Identify the parasite.
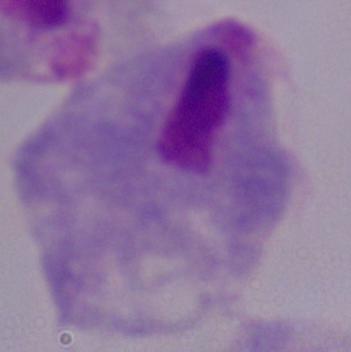
This is a trichomonad.

Photomicrograph. 1000x magnification.